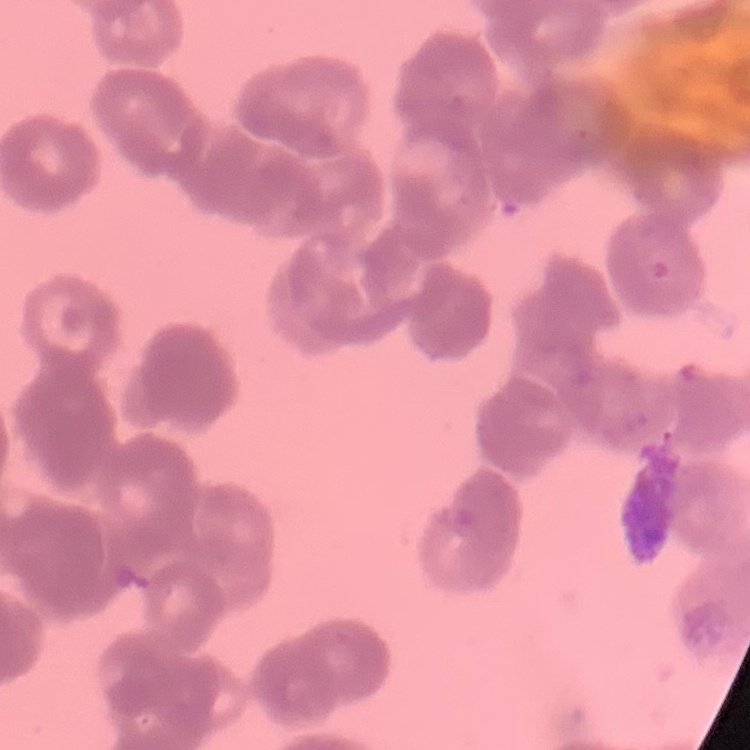

The red blood cells exhibit rouleaux formation. Stained with either Field's or Giemsa. One tile cut from a larger photomicrograph. Thin blood smear.